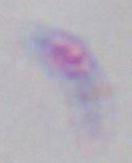

modality = micrograph
identification = Toxoplasma gondii
magnification = 1000x